Name the blood parasite species.
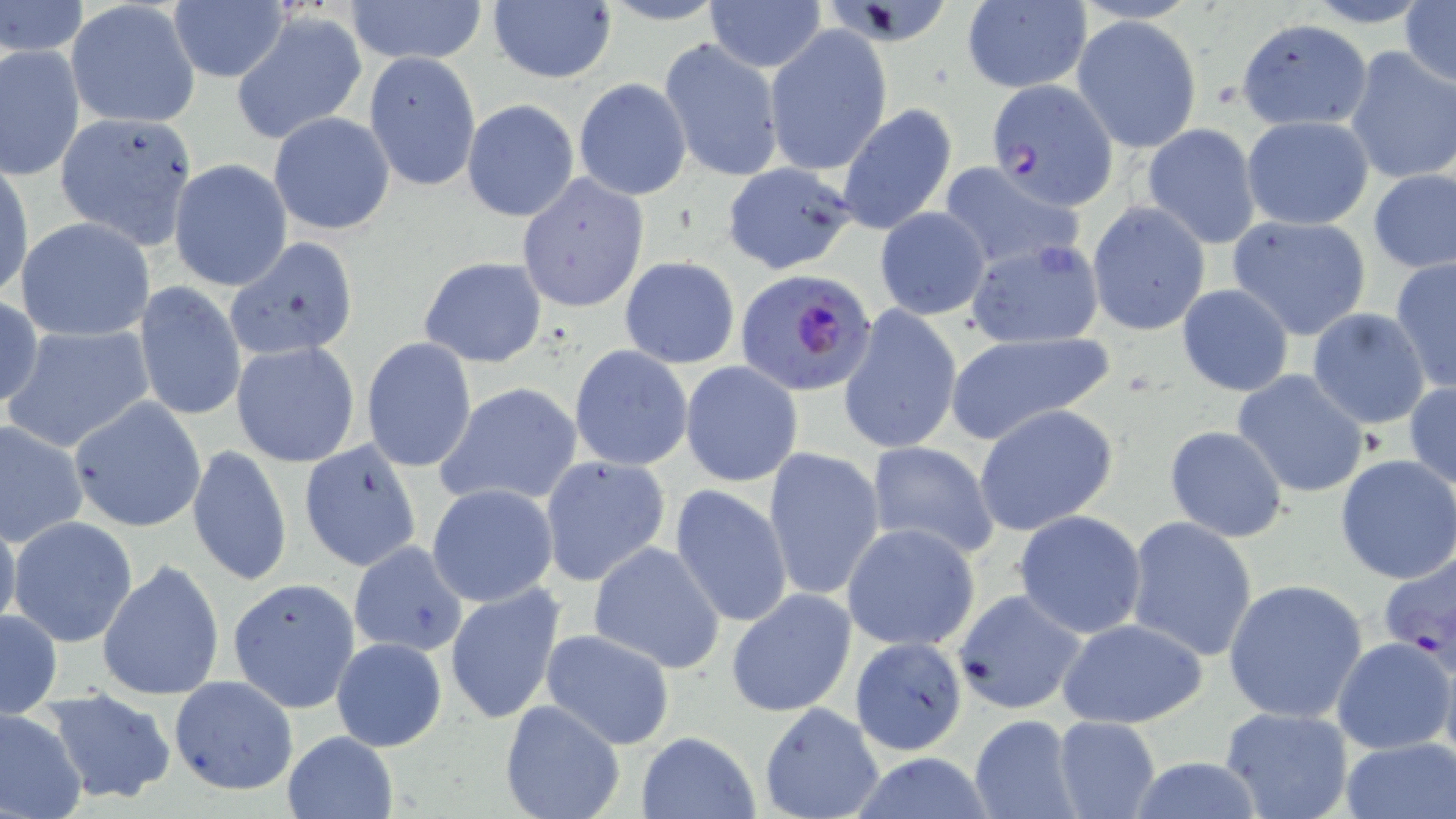

Plasmodium falciparum.

modality = optical microscopy
image size = 1456×819 pixels
stain = May-Grünwald-Giemsa
preparation = thin blood film
uninfected red blood cell locations = approximate bounding boxes as (x1,y1)-(x2,y2) corner pairs in pixels: (0,0)-(89,57), (1401,0)-(1456,89), (348,1)-(485,67), (703,1)-(828,71), (960,1)-(1092,93), (66,2)-(200,129), (168,2)-(289,84), (485,2)-(618,84), (231,12)-(369,146), (1071,14)-(1202,154), (1239,17)-(1372,130), (764,25)-(893,176), (659,38)-(783,184), (1,42)-(85,180), (1344,46)-(1455,185), (363,51)-(481,192), (573,78)-(691,201), (462,99)-(579,221), (836,104)-(957,236), (268,111)-(395,236), (52,115)-(200,259), (1241,115)-(1374,231), (1141,123)-(1261,247), (168,160)-(292,292), (0,161)-(34,303), (936,161)-(1085,271), (721,163)-(858,276), (1369,170)-(1456,273), (516,173)-(650,314), (1087,201)-(1211,336), (874,207)-(991,319), (1227,214)-(1372,340), (16,217)-(154,342), (225,236)-(359,360), (966,240)-(1104,349), (419,256)-(547,368), (619,256)-(740,369), (1389,258)-(1455,394), (133,282)-(246,422), (1175,285)-(1295,396), (0,296)-(45,410), (838,305)-(962,456), (1306,309)-(1432,429), (3,325)-(155,453), (945,332)-(1114,444), (361,338)-(478,473), (231,340)-(361,467), (568,345)-(693,472), (680,361)-(804,487), (1233,370)-(1369,499), (1404,379)-(1456,494), (437,382)-(584,506), (67,398)-(206,533), (973,404)-(1120,537), (0,419)-(88,546), (1164,424)-(1289,542), (297,438)-(423,574), (864,441)-(1000,560), (188,444)-(292,587), (763,446)-(885,603), (1334,453)-(1456,585), (539,454)-(670,585), (668,483)-(795,629), (427,484)-(561,608), (1013,510)-(1146,640), (0,511)-(21,639), (8,517)-(138,648), (1125,517)-(1259,662), (843,522)-(980,650), (348,541)-(469,660), (588,542)-(726,674), (1378,550)-(1456,672), (97,558)-(226,702), (228,578)-(361,713), (1223,578)-(1369,724), (444,583)-(568,729), (727,589)-(858,717), (952,590)-(1085,717), (0,608)-(63,720), (1059,617)-(1211,728), (539,629)-(678,749), (1332,635)-(1452,754), (331,637)-(447,752), (850,638)-(966,756), (1439,647)-(1456,780), (168,675)-(299,795), (44,686)-(179,806), (499,699)-(625,819), (758,703)-(886,819), (0,706)-(88,819), (1220,707)-(1353,819), (968,714)-(1082,819), (1053,716)-(1162,819), (283,731)-(398,818), (636,732)-(761,818), (1340,737)-(1456,818), (1119,757)-(1272,817)
Plasmodium falciparum-infected red blood cell locations = approximate bounding boxes as (x1,y1)-(x2,y2) corner pairs in pixels: (985,79)-(1117,211), (736,269)-(878,396)
magnification = 1000x
field of view = one of a larger specimen
platelet locations = approximate bounding boxes as (x1,y1)-(x2,y2) corner pairs in pixels: (1209,80)-(1244,112)